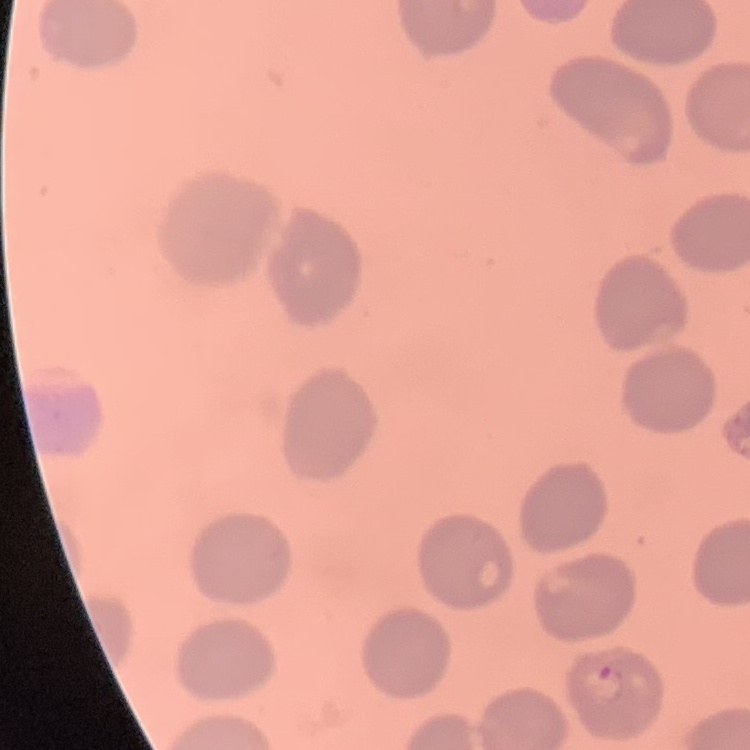 The red blood cells exhibit no rouleaux formation. One tile cut from a larger photomicrograph. Thin peripheral smear. Stained with either Field's or Giemsa.